Locate Plasmodium parasites and leukocytes.
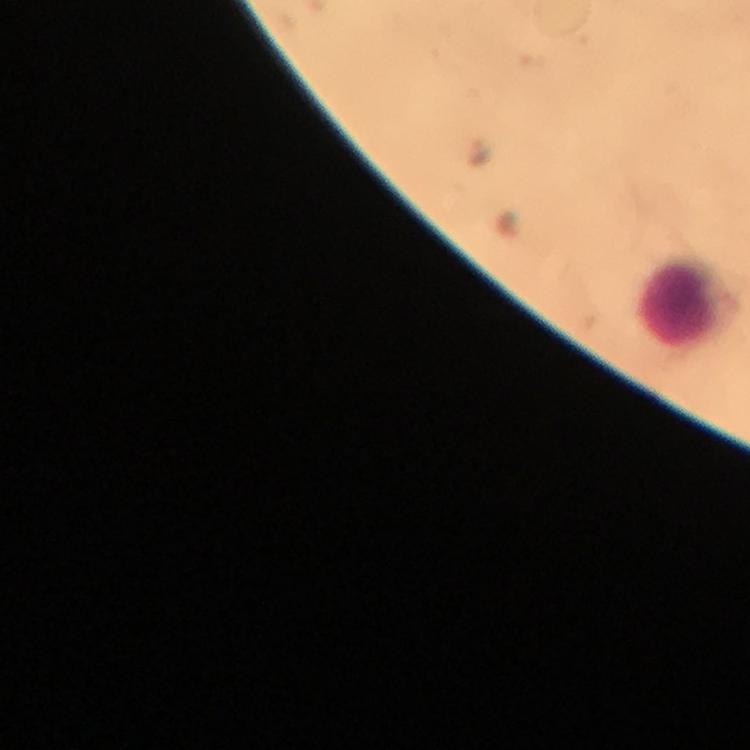

No Plasmodium parasites seen.
Approximate centers as [x, y] in pixels.
Leukocytes: [689, 303].

Immersion oil was used. 100x magnification. Image is 750×750 pixels. From a malaria diagnostic workup. Thick blood smear. Photographed through the microscope with a smartphone camera. Giemsa stain. Cropped region of a single field of view.